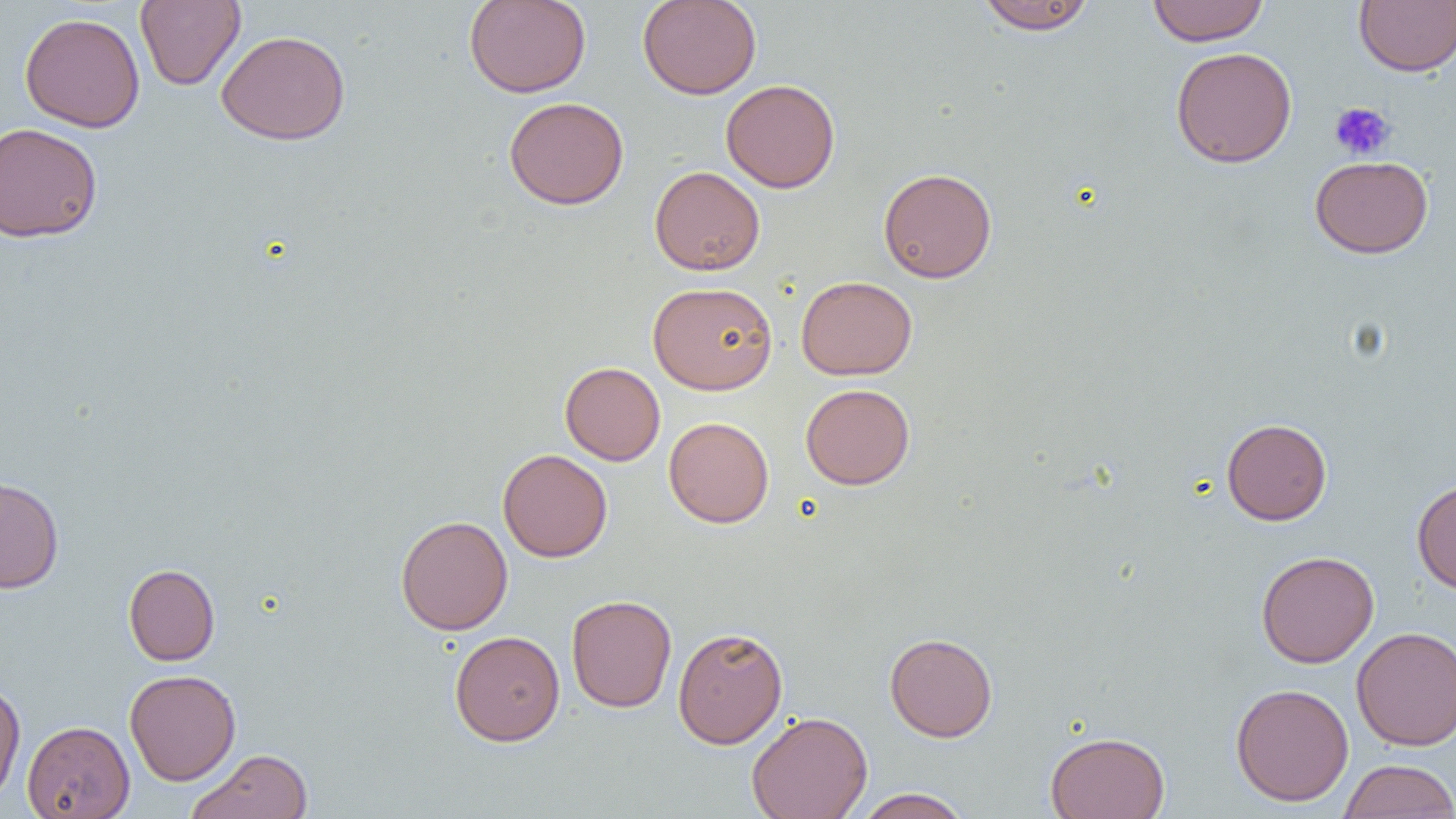

{
  "slide_level_diagnosis": "negative for blood parasites",
  "field_of_view": "single",
  "magnification": "1000x",
  "image_size": "1456×819 pixels",
  "platelet_locations": "approximate bounding boxes as (x1, y1, x2, y2) in pixels: (1329, 102, 1396, 161)",
  "uninfected_red_blood_cell_locations": "approximate bounding boxes as (x1, y1, x2, y2) in pixels: (135, 0, 245, 90), (463, 0, 591, 98), (637, 0, 762, 99), (1147, 0, 1269, 46), (975, 1, 1096, 34), (1354, 1, 1456, 77), (19, 12, 145, 133), (216, 29, 351, 146), (1170, 46, 1297, 168), (721, 79, 840, 193), (503, 97, 629, 210), (0, 122, 103, 243), (1309, 155, 1433, 258), (649, 166, 765, 275), (877, 167, 997, 283), (796, 275, 917, 380), (648, 281, 778, 394), (560, 362, 665, 465), (800, 383, 915, 490), (663, 417, 774, 528), (1221, 418, 1332, 525), (498, 449, 612, 562), (0, 475, 64, 593), (1411, 478, 1456, 594), (395, 515, 513, 635), (1255, 550, 1379, 668), (123, 563, 220, 665), (565, 594, 677, 712), (672, 626, 788, 749), (1352, 626, 1456, 750), (449, 630, 565, 746), (884, 632, 997, 742), (124, 669, 241, 786), (0, 680, 26, 806), (1230, 682, 1354, 806), (746, 711, 873, 819), (22, 720, 135, 818), (1045, 731, 1170, 819), (187, 749, 313, 819), (1337, 759, 1456, 819), (853, 788, 973, 818)",
  "modality": "optical microscopy",
  "preparation": "thin blood smear"
}